Classify this cell by malaria status.
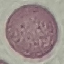

Uninfected.

Summary:
  - Image type: cell patch, automatically extracted from a larger field of view and resized to 64 × 64 pixels
  - Stain: Giemsa
  - Capture: smartphone camera at the microscope eyepiece
  - Preparation: thin smear